Report the malaria status of this cell.
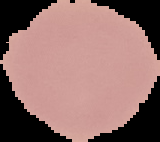
Uninfected.

image size = 160×142 pixels
preparation = thin blood smear
image type = cell region segmented out of the field of view; surrounding area masked to black